Classify this cell by malaria status.
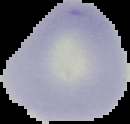
Uninfected.

Summary:
  - Preparation: thin blood film
  - Image type: segmented cell region on a black background
  - Image size: 130×124 pixels